Describe the morphology of the erythrocytes.
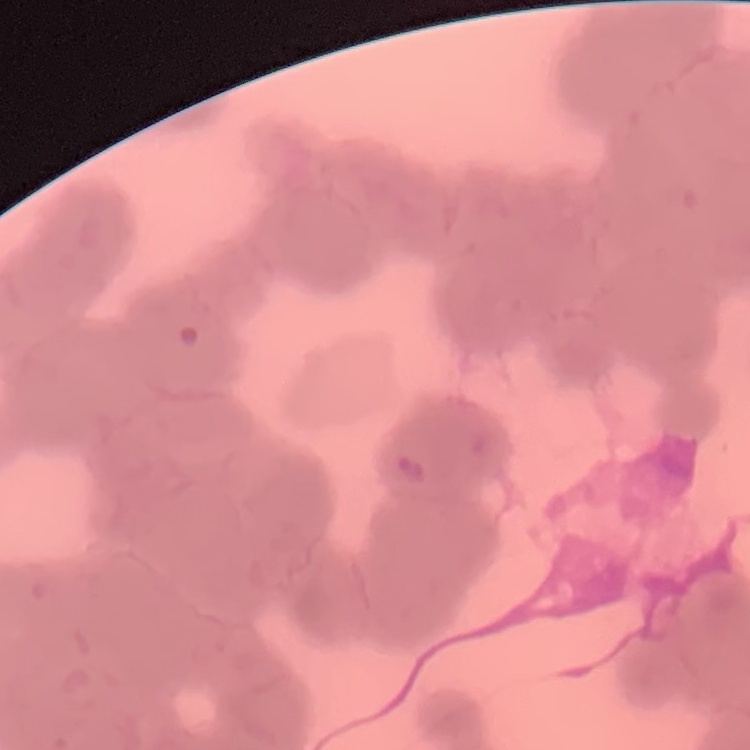
They show rouleaux formation.

Summary:
  - Image type: one tile cut from a larger photomicrograph
  - Preparation: thin blood smear
  - Stain: Field's or Giemsa